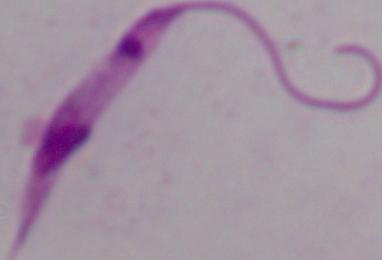

Summary:
  - Modality: photomicrograph
  - Identification: Leishmania
  - Magnification: 1000x